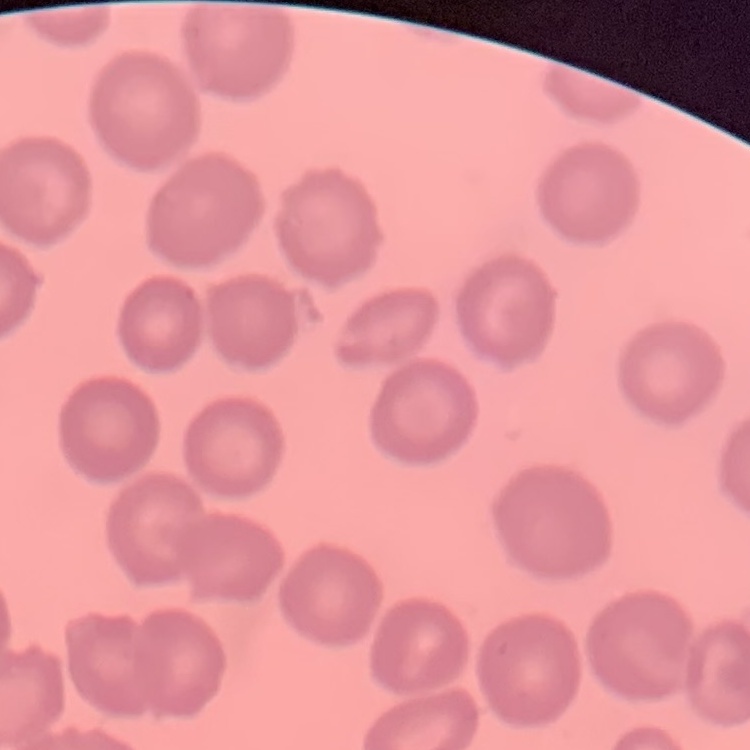
Summary:
  - Erythrocyte morphology: no rouleaux formation
  - Stain: Field's or Giemsa
  - Preparation: thin blood film
  - Image type: square crop of a larger photomicrograph